Give the position of each Plasmodium falciparum parasite with its life-cycle stage, each leukocyte, and any debris.
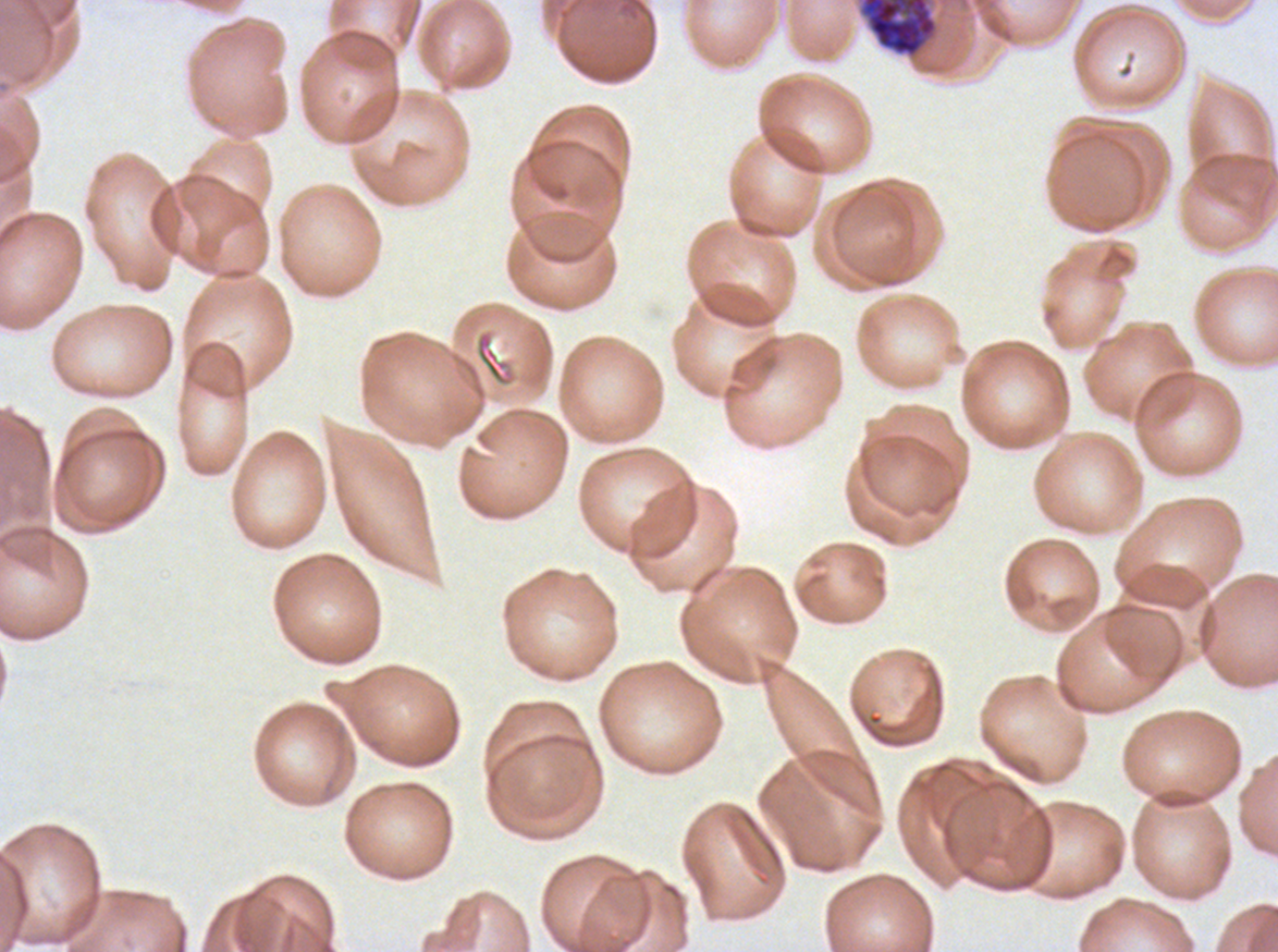
Approximate bounding boxes as [x1, y1, x2, y2] in pixels.
Segmenters: [857, 0, 940, 60].
No rings, late-ring/early-trophozoite forms, mid trophozoites, late trophozoites, early schizonts, late schizonts, gametocytes, leukocytes, or debris observed.

Summary:
  - Field of view: one sub-image of a larger composite
  - Specimen: ex-vivo Plasmodium falciparum culture from a patient in The Gambia, grown for 24 to 48 hours
  - Stain: Giemsa
  - Preparation: thin blood smear
  - Image size: 1278×952 pixels